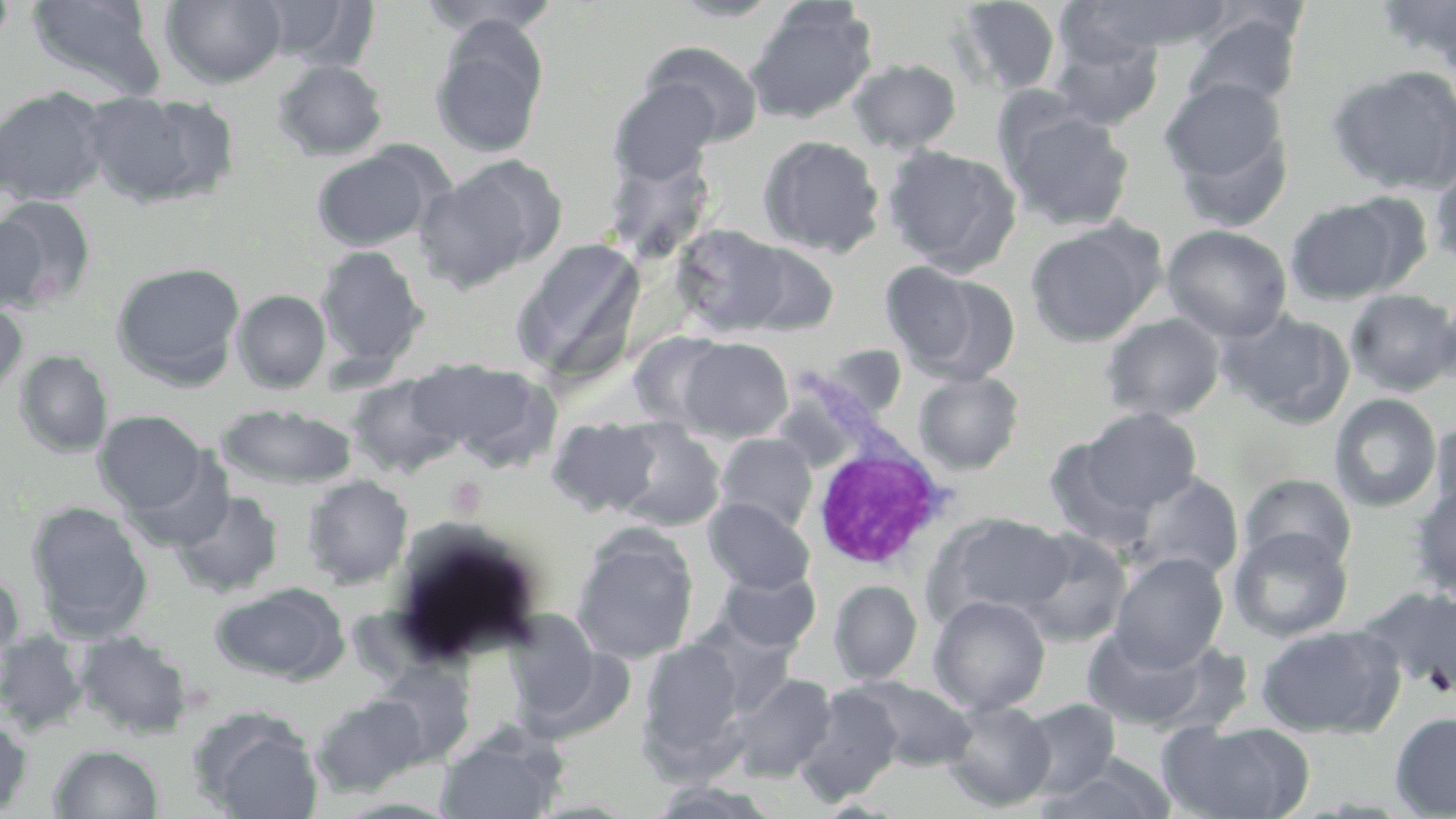

Approximate bounding boxes as named x1/y1/x2/y2 corners in pixels. Uninfected red blood cell locations: (x1=26, y1=0, x2=167, y2=101), (x1=161, y1=0, x2=288, y2=89), (x1=417, y1=0, x2=561, y2=36), (x1=667, y1=0, x2=787, y2=22), (x1=1375, y1=0, x2=1456, y2=70), (x1=1, y1=1, x2=17, y2=53), (x1=258, y1=1, x2=375, y2=69), (x1=950, y1=1, x2=1064, y2=98), (x1=1067, y1=1, x2=1236, y2=56), (x1=745, y1=2, x2=877, y2=124), (x1=1182, y1=11, x2=1303, y2=115), (x1=430, y1=21, x2=548, y2=159), (x1=1048, y1=35, x2=1164, y2=132), (x1=643, y1=42, x2=764, y2=146), (x1=848, y1=58, x2=961, y2=154), (x1=273, y1=59, x2=388, y2=161), (x1=1325, y1=65, x2=1456, y2=195), (x1=1158, y1=77, x2=1293, y2=219), (x1=609, y1=80, x2=720, y2=186), (x1=0, y1=87, x2=110, y2=206), (x1=82, y1=90, x2=238, y2=209), (x1=1000, y1=103, x2=1136, y2=231), (x1=757, y1=135, x2=885, y2=257), (x1=601, y1=138, x2=718, y2=264), (x1=310, y1=145, x2=443, y2=252), (x1=883, y1=145, x2=1022, y2=274), (x1=416, y1=157, x2=564, y2=292), (x1=1428, y1=162, x2=1456, y2=270), (x1=0, y1=195, x2=98, y2=308), (x1=1286, y1=198, x2=1406, y2=304), (x1=0, y1=212, x2=50, y2=313), (x1=1024, y1=218, x2=1166, y2=346), (x1=671, y1=224, x2=792, y2=336), (x1=1161, y1=224, x2=1293, y2=341), (x1=511, y1=237, x2=647, y2=382), (x1=734, y1=241, x2=840, y2=336), (x1=315, y1=245, x2=430, y2=375), (x1=111, y1=261, x2=246, y2=387), (x1=899, y1=269, x2=1021, y2=385), (x1=233, y1=289, x2=331, y2=393), (x1=1345, y1=289, x2=1456, y2=396), (x1=0, y1=299, x2=28, y2=399), (x1=1218, y1=308, x2=1355, y2=427), (x1=1100, y1=312, x2=1226, y2=422), (x1=629, y1=331, x2=732, y2=431), (x1=679, y1=337, x2=793, y2=441), (x1=803, y1=344, x2=907, y2=424), (x1=15, y1=350, x2=113, y2=458), (x1=417, y1=358, x2=561, y2=472), (x1=912, y1=370, x2=1025, y2=475), (x1=346, y1=373, x2=467, y2=477), (x1=1329, y1=393, x2=1441, y2=513), (x1=217, y1=403, x2=357, y2=491), (x1=1079, y1=407, x2=1204, y2=513), (x1=95, y1=410, x2=207, y2=513), (x1=547, y1=417, x2=664, y2=517), (x1=1429, y1=419, x2=1456, y2=520), (x1=610, y1=422, x2=727, y2=532), (x1=715, y1=433, x2=818, y2=533), (x1=1043, y1=437, x2=1161, y2=552), (x1=125, y1=453, x2=236, y2=553), (x1=1125, y1=472, x2=1244, y2=581), (x1=303, y1=474, x2=413, y2=588), (x1=1239, y1=474, x2=1357, y2=571), (x1=1409, y1=484, x2=1456, y2=601), (x1=172, y1=490, x2=283, y2=597), (x1=704, y1=497, x2=815, y2=594), (x1=27, y1=502, x2=153, y2=641), (x1=928, y1=512, x2=1072, y2=623), (x1=1228, y1=527, x2=1353, y2=643), (x1=1014, y1=529, x2=1131, y2=647), (x1=573, y1=534, x2=698, y2=664), (x1=1109, y1=552, x2=1229, y2=670), (x1=0, y1=568, x2=24, y2=671), (x1=715, y1=569, x2=821, y2=653), (x1=829, y1=579, x2=923, y2=685), (x1=209, y1=581, x2=349, y2=682), (x1=1360, y1=587, x2=1456, y2=698), (x1=928, y1=595, x2=1050, y2=715), (x1=503, y1=615, x2=619, y2=734), (x1=688, y1=617, x2=801, y2=716), (x1=1255, y1=623, x2=1405, y2=738), (x1=1083, y1=625, x2=1238, y2=734), (x1=0, y1=631, x2=88, y2=734), (x1=74, y1=631, x2=193, y2=738), (x1=639, y1=639, x2=747, y2=768), (x1=371, y1=663, x2=476, y2=766), (x1=731, y1=673, x2=838, y2=781), (x1=851, y1=678, x2=977, y2=772), (x1=795, y1=685, x2=903, y2=804), (x1=312, y1=693, x2=429, y2=796), (x1=940, y1=699, x2=1056, y2=812), (x1=1016, y1=699, x2=1122, y2=799), (x1=1389, y1=711, x2=1456, y2=817), (x1=0, y1=718, x2=32, y2=816), (x1=1162, y1=720, x2=1315, y2=819), (x1=199, y1=721, x2=324, y2=819), (x1=436, y1=728, x2=568, y2=819), (x1=49, y1=744, x2=164, y2=819), (x1=1037, y1=755, x2=1177, y2=819), (x1=644, y1=780, x2=783, y2=818). White blood cell locations: (x1=807, y1=442, x2=956, y2=571). Slide-level diagnosis: negative for blood parasites. Captured at 1000x magnification. Single field of view. Image is 1456×819 pixels. Light microscopy. Thin blood smear. May-Grünwald-Giemsa stain.